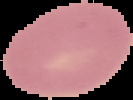
image size = 133×100 pixels
malaria status = uninfected
preparation = thin blood smear
image type = segmented cell region on a black background